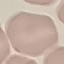 Malaria status: uninfected. Photographed with a smartphone camera at the microscope eyepiece. Cell patch, automatically extracted from a larger field of view and resized to 64 × 64 pixels. Giemsa stain. Thin smear of blood.